Locate and identify every blood parasite.
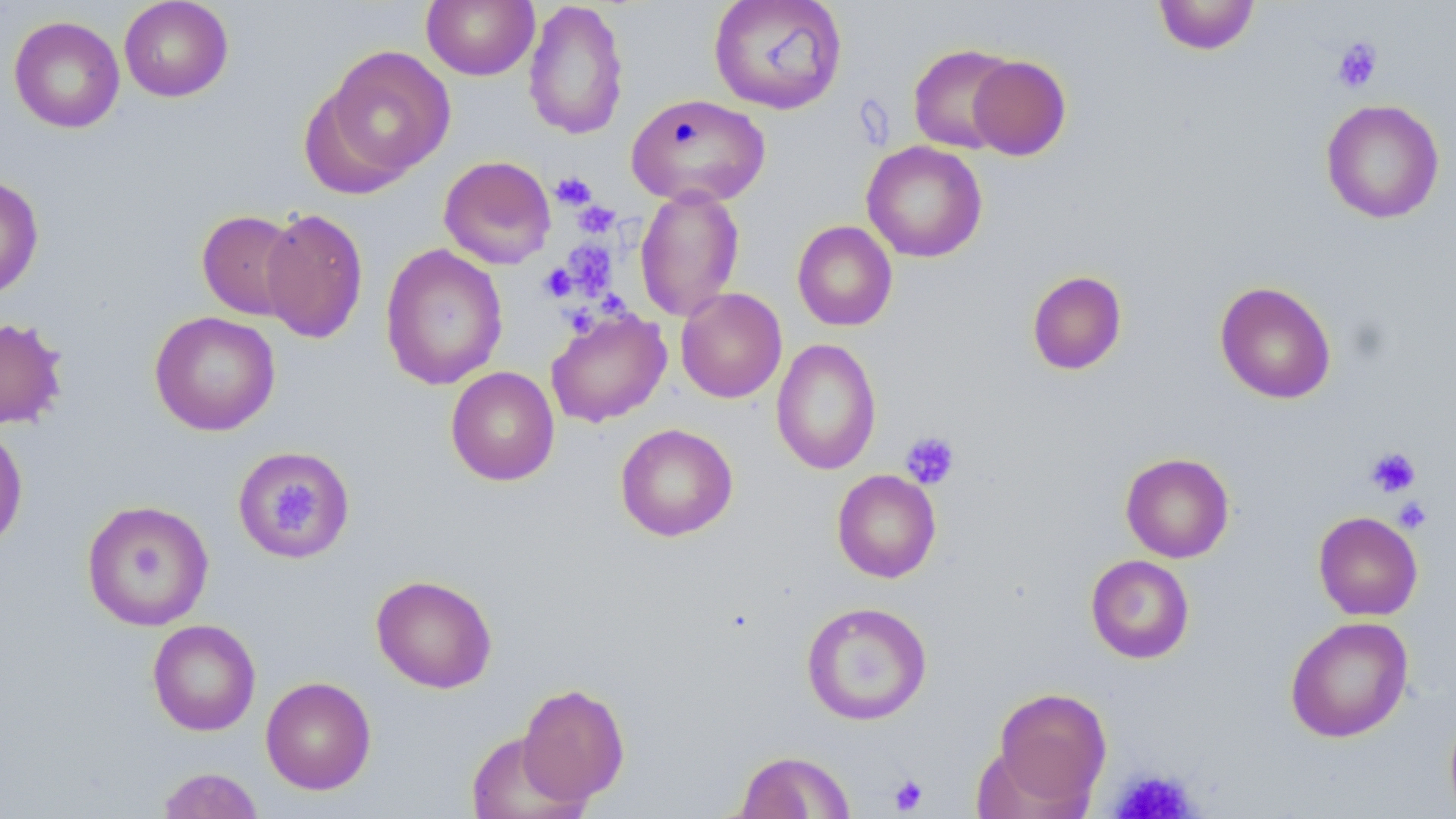
No blood parasites observed.

Summary:
  - Coordinate format: approximate bounding boxes as [x1, y1, x2, y2] in pixels
  - Uninfected red blood cell locations: [118, 0, 233, 102], [421, 0, 539, 80], [523, 0, 629, 141], [708, 0, 848, 115], [1152, 0, 1261, 55], [8, 15, 125, 133], [320, 44, 455, 186], [908, 44, 1019, 154], [967, 55, 1071, 161], [626, 93, 771, 208], [1320, 99, 1445, 224], [861, 141, 988, 262], [439, 155, 556, 270], [0, 174, 44, 299], [634, 186, 745, 322], [259, 207, 369, 344], [196, 210, 303, 321], [792, 220, 897, 331], [380, 243, 508, 390], [1026, 270, 1127, 375], [1215, 281, 1336, 404], [676, 287, 787, 403], [545, 308, 671, 428], [149, 310, 281, 436], [0, 316, 68, 430], [771, 338, 882, 475], [445, 367, 559, 486], [0, 423, 28, 550], [615, 423, 738, 542], [233, 446, 354, 561], [1120, 452, 1235, 563], [832, 469, 941, 583], [81, 499, 215, 631], [1313, 511, 1423, 620], [1085, 554, 1195, 664], [370, 574, 497, 693], [801, 601, 932, 725], [1284, 616, 1414, 743], [147, 619, 261, 736], [260, 676, 377, 795], [516, 682, 630, 806], [991, 686, 1111, 808], [1444, 704, 1456, 819], [464, 730, 584, 819], [735, 750, 856, 818], [156, 766, 265, 818]
  - Platelet locations: [1331, 37, 1382, 93], [550, 172, 596, 211], [573, 201, 620, 237], [561, 240, 618, 299], [539, 263, 577, 302], [598, 292, 639, 330], [561, 304, 601, 340], [899, 431, 960, 490], [1366, 447, 1421, 497], [275, 482, 320, 538], [1393, 496, 1433, 533], [1108, 767, 1201, 819], [889, 774, 929, 814]
  - Slide-level diagnosis: no evidence of blood parasites
  - Image size: 1456×819 pixels
  - Preparation: thin blood film
  - Magnification: 1000x
  - Stain: May-Grünwald-Giemsa
  - Modality: optical microscopy
  - Field of view: one of a larger specimen